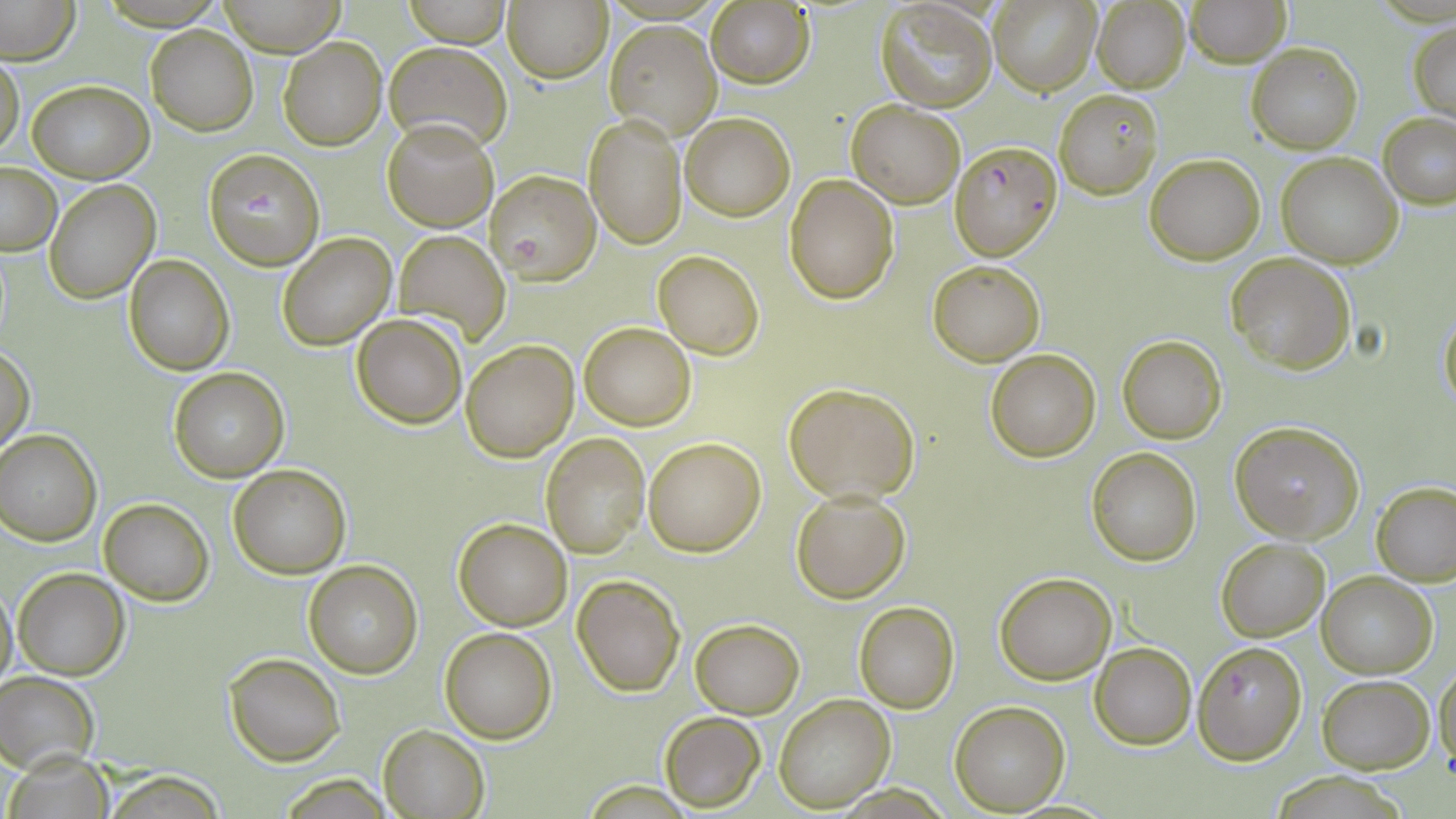
Plasmodium falciparum-infected red blood cell locations = approximate bounding boxes as named x1/y1/x2/y2 corners in pixels: (x1=951, y1=141, x2=1061, y2=260), (x1=203, y1=147, x2=326, y2=270), (x1=485, y1=168, x2=602, y2=285), (x1=1191, y1=639, x2=1307, y2=765)
slide-level diagnosis = Plasmodium falciparum
stain = May-Grünwald-Giemsa
magnification = 1000x
modality = optical microscopy
uninfected red blood cell locations = approximate bounding boxes as named x1/y1/x2/y2 corners in pixels: (x1=0, y1=0, x2=79, y2=64), (x1=217, y1=0, x2=345, y2=55), (x1=406, y1=0, x2=511, y2=47), (x1=502, y1=0, x2=612, y2=84), (x1=705, y1=0, x2=814, y2=89), (x1=988, y1=0, x2=1102, y2=97), (x1=1186, y1=0, x2=1291, y2=67), (x1=1091, y1=1, x2=1191, y2=94), (x1=875, y1=2, x2=997, y2=114), (x1=603, y1=18, x2=723, y2=139), (x1=1407, y1=18, x2=1454, y2=122), (x1=147, y1=27, x2=258, y2=135), (x1=278, y1=36, x2=387, y2=151), (x1=384, y1=40, x2=510, y2=153), (x1=1247, y1=41, x2=1363, y2=152), (x1=0, y1=51, x2=25, y2=159), (x1=27, y1=79, x2=153, y2=183), (x1=1054, y1=89, x2=1162, y2=199), (x1=846, y1=99, x2=965, y2=207), (x1=679, y1=110, x2=795, y2=221), (x1=583, y1=112, x2=687, y2=250), (x1=1379, y1=112, x2=1456, y2=208), (x1=383, y1=119, x2=498, y2=232), (x1=1276, y1=151, x2=1403, y2=269), (x1=1145, y1=153, x2=1266, y2=263), (x1=1, y1=161, x2=61, y2=256), (x1=785, y1=173, x2=899, y2=303), (x1=44, y1=180, x2=159, y2=303), (x1=394, y1=231, x2=510, y2=339), (x1=277, y1=233, x2=396, y2=350), (x1=653, y1=250, x2=764, y2=358), (x1=1226, y1=252, x2=1356, y2=373), (x1=124, y1=256, x2=234, y2=375), (x1=928, y1=259, x2=1045, y2=367), (x1=1438, y1=305, x2=1456, y2=412), (x1=351, y1=314, x2=467, y2=428), (x1=579, y1=322, x2=696, y2=430), (x1=1116, y1=334, x2=1226, y2=443), (x1=461, y1=340, x2=577, y2=461), (x1=1, y1=343, x2=35, y2=457), (x1=985, y1=350, x2=1101, y2=462), (x1=167, y1=366, x2=290, y2=481), (x1=783, y1=383, x2=919, y2=502), (x1=1230, y1=420, x2=1366, y2=542), (x1=0, y1=429, x2=101, y2=545), (x1=540, y1=433, x2=650, y2=558), (x1=642, y1=437, x2=764, y2=556), (x1=1086, y1=447, x2=1201, y2=565), (x1=228, y1=464, x2=352, y2=578), (x1=1373, y1=480, x2=1456, y2=586), (x1=789, y1=488, x2=910, y2=603), (x1=98, y1=498, x2=214, y2=604), (x1=454, y1=518, x2=572, y2=630), (x1=1216, y1=537, x2=1329, y2=640), (x1=302, y1=562, x2=422, y2=678), (x1=12, y1=568, x2=129, y2=679), (x1=1317, y1=571, x2=1438, y2=678), (x1=994, y1=574, x2=1117, y2=684), (x1=572, y1=575, x2=684, y2=696), (x1=0, y1=581, x2=17, y2=693), (x1=853, y1=603, x2=959, y2=713), (x1=690, y1=618, x2=804, y2=717), (x1=440, y1=627, x2=558, y2=743), (x1=1090, y1=643, x2=1195, y2=749), (x1=223, y1=651, x2=347, y2=767), (x1=1432, y1=662, x2=1456, y2=780), (x1=0, y1=672, x2=99, y2=772), (x1=1318, y1=675, x2=1434, y2=772), (x1=773, y1=694, x2=895, y2=813), (x1=951, y1=701, x2=1070, y2=815), (x1=660, y1=712, x2=766, y2=811), (x1=377, y1=723, x2=488, y2=817), (x1=5, y1=751, x2=113, y2=817), (x1=104, y1=772, x2=229, y2=817), (x1=1272, y1=773, x2=1405, y2=817)
preparation = thin blood film
image size = 1456×819 pixels
field of view = single